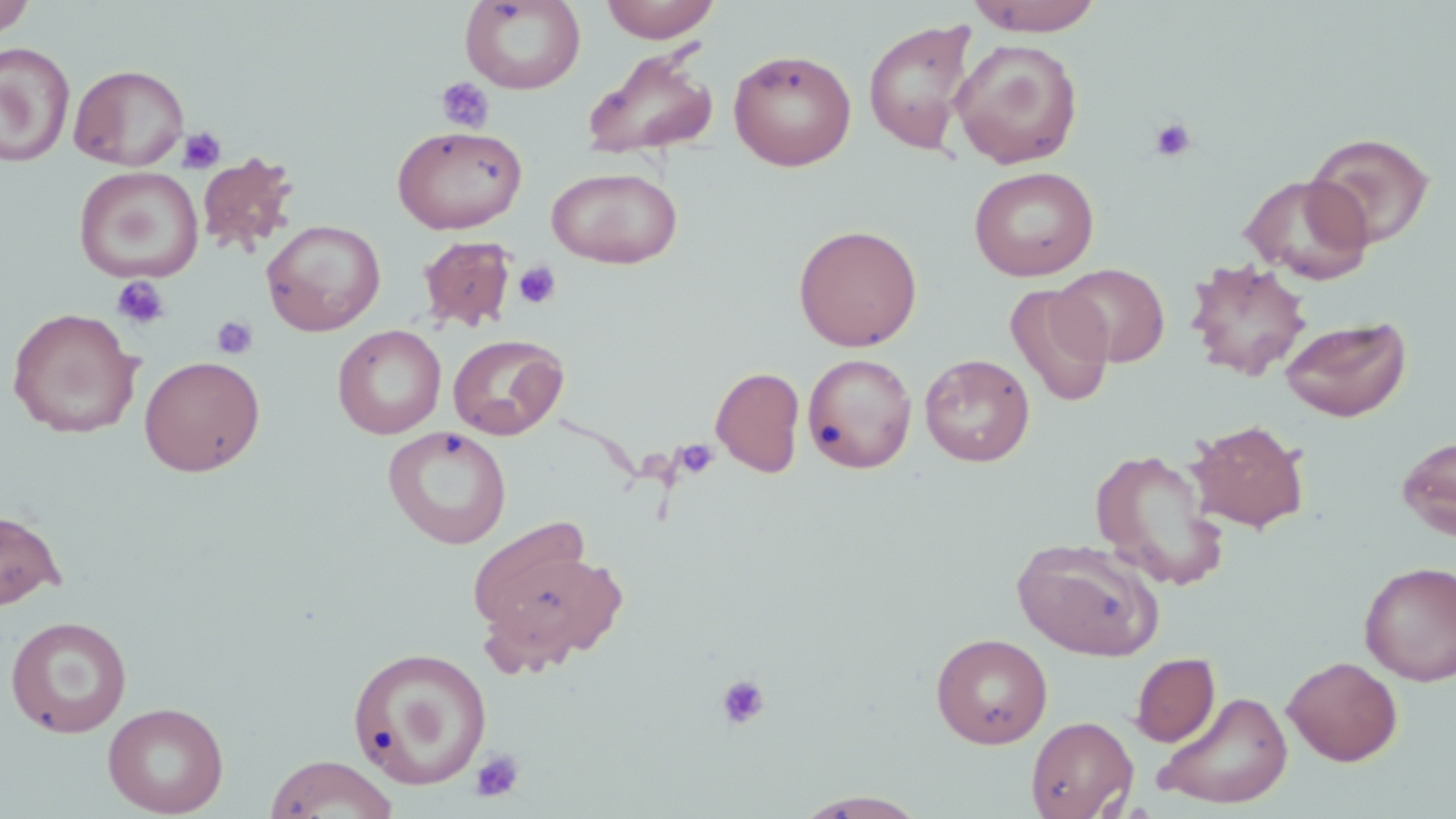

Summary:
  - Coordinate format: approximate bounding boxes as named x1/y1/x2/y2 corners in pixels
  - Uninfected red blood cell locations: (x1=0, y1=0, x2=37, y2=39), (x1=460, y1=0, x2=586, y2=94), (x1=599, y1=0, x2=721, y2=43), (x1=965, y1=0, x2=1106, y2=35), (x1=862, y1=17, x2=978, y2=155), (x1=950, y1=38, x2=1084, y2=169), (x1=0, y1=41, x2=75, y2=167), (x1=582, y1=48, x2=719, y2=160), (x1=728, y1=48, x2=857, y2=171), (x1=70, y1=63, x2=190, y2=171), (x1=391, y1=124, x2=527, y2=234), (x1=1305, y1=132, x2=1436, y2=250), (x1=197, y1=152, x2=300, y2=256), (x1=968, y1=165, x2=1099, y2=281), (x1=74, y1=166, x2=204, y2=283), (x1=547, y1=166, x2=683, y2=268), (x1=1240, y1=173, x2=1375, y2=285), (x1=262, y1=219, x2=386, y2=336), (x1=793, y1=223, x2=923, y2=351), (x1=417, y1=234, x2=518, y2=333), (x1=1185, y1=259, x2=1312, y2=381), (x1=1054, y1=264, x2=1169, y2=368), (x1=1005, y1=284, x2=1115, y2=408), (x1=6, y1=307, x2=143, y2=439), (x1=1280, y1=315, x2=1412, y2=422), (x1=332, y1=324, x2=446, y2=439), (x1=447, y1=333, x2=569, y2=441), (x1=802, y1=352, x2=918, y2=474), (x1=919, y1=353, x2=1035, y2=466), (x1=139, y1=355, x2=266, y2=477), (x1=711, y1=366, x2=806, y2=478), (x1=1188, y1=419, x2=1309, y2=532), (x1=383, y1=426, x2=513, y2=549), (x1=1396, y1=433, x2=1456, y2=541), (x1=1089, y1=448, x2=1231, y2=591), (x1=0, y1=509, x2=66, y2=610), (x1=470, y1=527, x2=621, y2=667), (x1=1011, y1=537, x2=1164, y2=661), (x1=1358, y1=560, x2=1456, y2=686), (x1=5, y1=616, x2=133, y2=738), (x1=931, y1=632, x2=1053, y2=748), (x1=347, y1=646, x2=493, y2=791), (x1=1130, y1=652, x2=1220, y2=747), (x1=1282, y1=656, x2=1403, y2=766), (x1=1154, y1=690, x2=1294, y2=809), (x1=102, y1=702, x2=229, y2=817), (x1=1026, y1=715, x2=1138, y2=818), (x1=264, y1=753, x2=399, y2=818), (x1=794, y1=790, x2=931, y2=818)
  - Platelet locations: (x1=436, y1=77, x2=494, y2=134), (x1=1149, y1=116, x2=1198, y2=163), (x1=178, y1=127, x2=226, y2=174), (x1=512, y1=260, x2=562, y2=310), (x1=111, y1=275, x2=171, y2=330), (x1=211, y1=315, x2=258, y2=359), (x1=674, y1=438, x2=720, y2=480), (x1=716, y1=673, x2=771, y2=731), (x1=470, y1=748, x2=525, y2=802)
  - Slide-level diagnosis: negative for blood parasites
  - Preparation: thin blood smear
  - Image size: 1456×819 pixels
  - Magnification: 1000x
  - Field of view: one of a larger specimen
  - Modality: optical microscopy
  - Stain: May-Grünwald-Giemsa